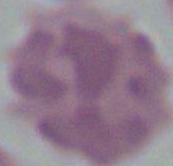
Summary:
  - Magnification: 1000x
  - Modality: micrograph
  - Identification: red blood cell